Classify this cell by malaria status.
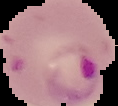

Parasitized.

From a thin blood smear. Segmented cell region on a black background. Image is 118×106 pixels.